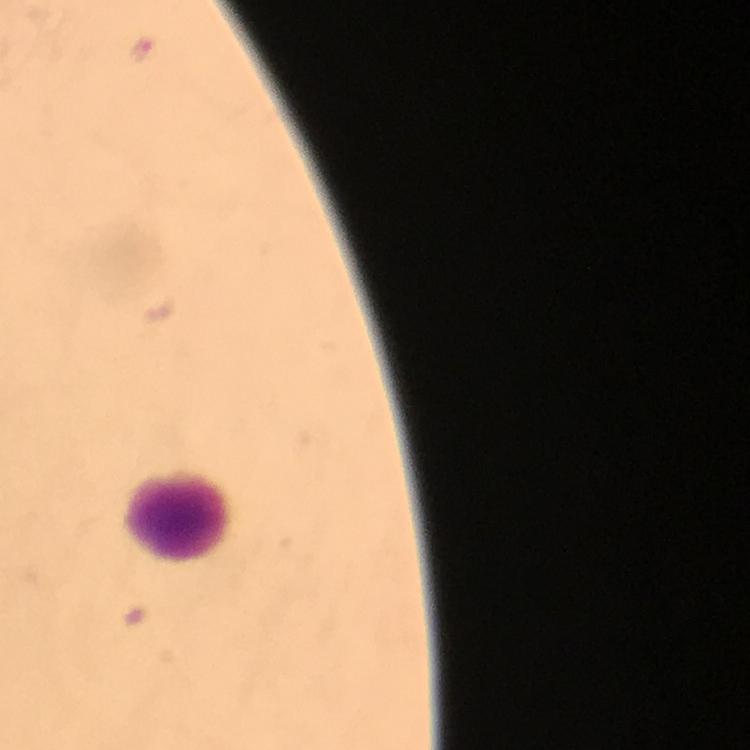
Approximate centers as [x, y] in pixels. Leukocyte locations: [178, 514]. Plasmodium parasite locations: [143, 49]. Photographed with a smartphone mounted on the microscope. 100x magnification. From a diagnostic examination for malaria. Thick blood smear. Immersion oil applied. Giemsa stain. Image is 750×750 pixels. A crop from one field of view.